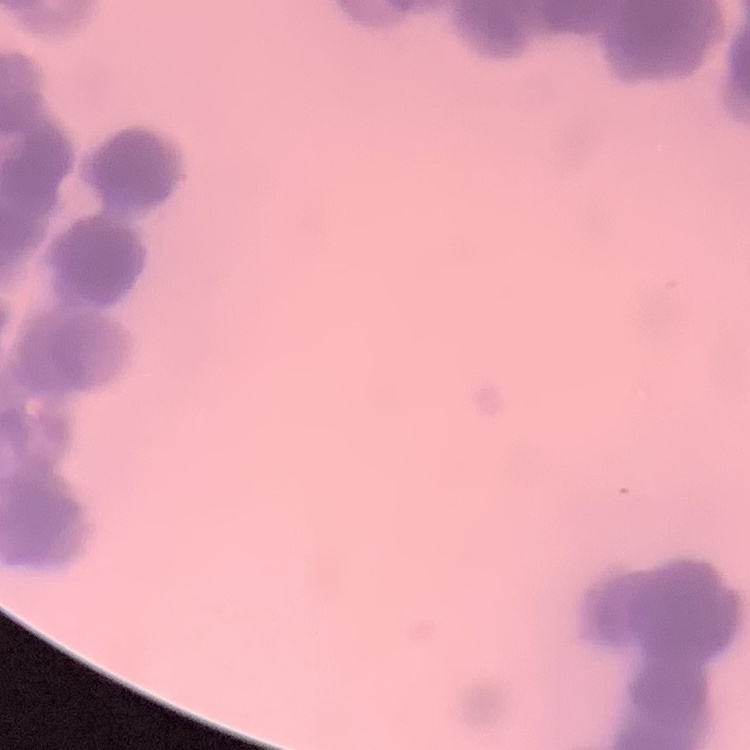

The erythrocytes exhibit rouleaux formation. Thin blood film. Square crop of a larger photomicrograph. Stained with either Field's or Giemsa.